Assess this cell for malaria.
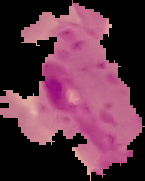
Parasitized.

Cell region segmented out of the field of view; the surrounding area is masked to black. Image is 145×181 pixels. From a thin blood film.